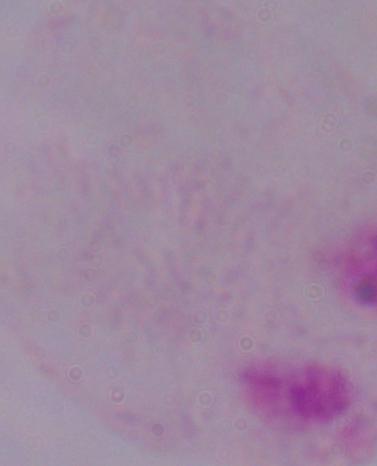
Captured at 1000x magnification. Micrograph. A trichomonad is seen.